Outline each Plasmodium vivax-infected red blood cell.
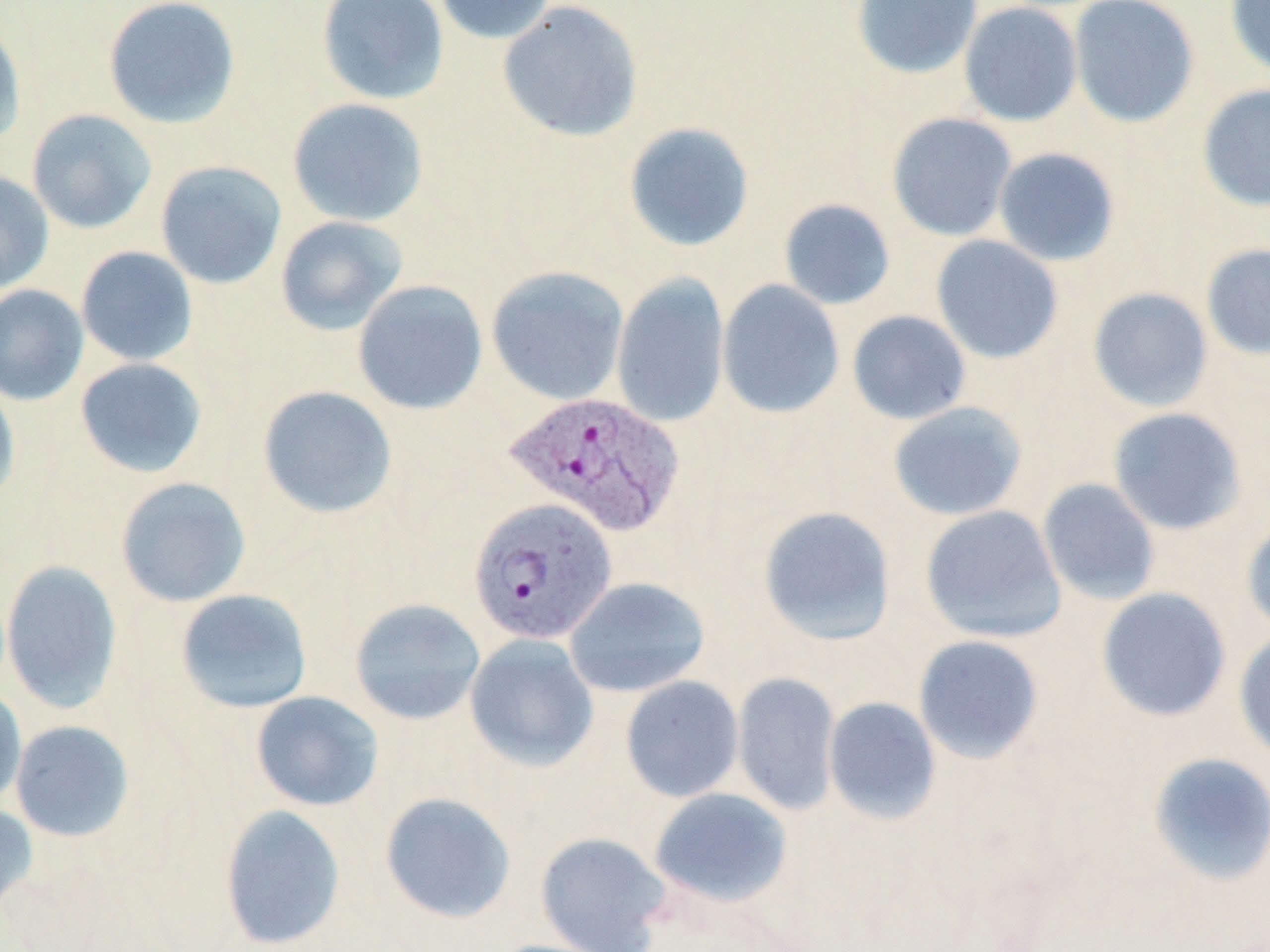

Approximate bounding boxes as named x1/y1/x2/y2 corners in pixels.
Plasmodium vivax-infected red blood cells: (x1=502, y1=391, x2=686, y2=537), (x1=469, y1=498, x2=617, y2=646).

Uninfected red blood cell locations: (x1=102, y1=0, x2=241, y2=130), (x1=317, y1=0, x2=450, y2=106), (x1=432, y1=0, x2=558, y2=45), (x1=850, y1=0, x2=984, y2=80), (x1=1068, y1=0, x2=1200, y2=128), (x1=1224, y1=0, x2=1270, y2=79), (x1=497, y1=1, x2=644, y2=142), (x1=958, y1=2, x2=1083, y2=127), (x1=0, y1=15, x2=27, y2=150), (x1=1196, y1=83, x2=1270, y2=212), (x1=287, y1=98, x2=429, y2=227), (x1=26, y1=108, x2=157, y2=234), (x1=886, y1=112, x2=1017, y2=242), (x1=622, y1=121, x2=755, y2=252), (x1=993, y1=147, x2=1121, y2=266), (x1=155, y1=161, x2=287, y2=289), (x1=0, y1=170, x2=54, y2=294), (x1=778, y1=198, x2=897, y2=310), (x1=275, y1=215, x2=408, y2=336), (x1=930, y1=234, x2=1064, y2=364), (x1=1201, y1=242, x2=1270, y2=362), (x1=76, y1=246, x2=198, y2=366), (x1=486, y1=266, x2=629, y2=406), (x1=611, y1=273, x2=731, y2=429), (x1=352, y1=279, x2=488, y2=415), (x1=717, y1=280, x2=845, y2=419), (x1=0, y1=284, x2=89, y2=406), (x1=1087, y1=287, x2=1214, y2=413), (x1=846, y1=310, x2=971, y2=425), (x1=74, y1=357, x2=208, y2=479), (x1=0, y1=377, x2=20, y2=509), (x1=257, y1=385, x2=398, y2=519), (x1=887, y1=401, x2=1028, y2=521), (x1=1107, y1=407, x2=1246, y2=535), (x1=115, y1=477, x2=251, y2=607), (x1=1037, y1=478, x2=1160, y2=605), (x1=757, y1=505, x2=897, y2=646), (x1=920, y1=505, x2=1066, y2=644), (x1=1241, y1=514, x2=1270, y2=637), (x1=1, y1=559, x2=123, y2=714), (x1=564, y1=576, x2=710, y2=698), (x1=1096, y1=587, x2=1231, y2=722), (x1=175, y1=589, x2=312, y2=714), (x1=349, y1=598, x2=485, y2=726), (x1=1234, y1=629, x2=1270, y2=762), (x1=464, y1=633, x2=599, y2=772), (x1=913, y1=635, x2=1044, y2=764), (x1=732, y1=671, x2=842, y2=816), (x1=620, y1=675, x2=744, y2=802), (x1=0, y1=687, x2=27, y2=809), (x1=250, y1=691, x2=384, y2=812), (x1=823, y1=696, x2=942, y2=825), (x1=10, y1=720, x2=134, y2=842), (x1=1146, y1=751, x2=1270, y2=886), (x1=648, y1=787, x2=793, y2=907), (x1=379, y1=791, x2=517, y2=924), (x1=0, y1=801, x2=38, y2=919), (x1=219, y1=804, x2=346, y2=950), (x1=535, y1=831, x2=672, y2=952). Slide-level diagnosis: Plasmodium vivax. Captured at 1000x magnification. May-Grünwald-Giemsa stain. Image is 1270×952 pixels. Thin blood smear. One field of a larger specimen. Optical microscopy.